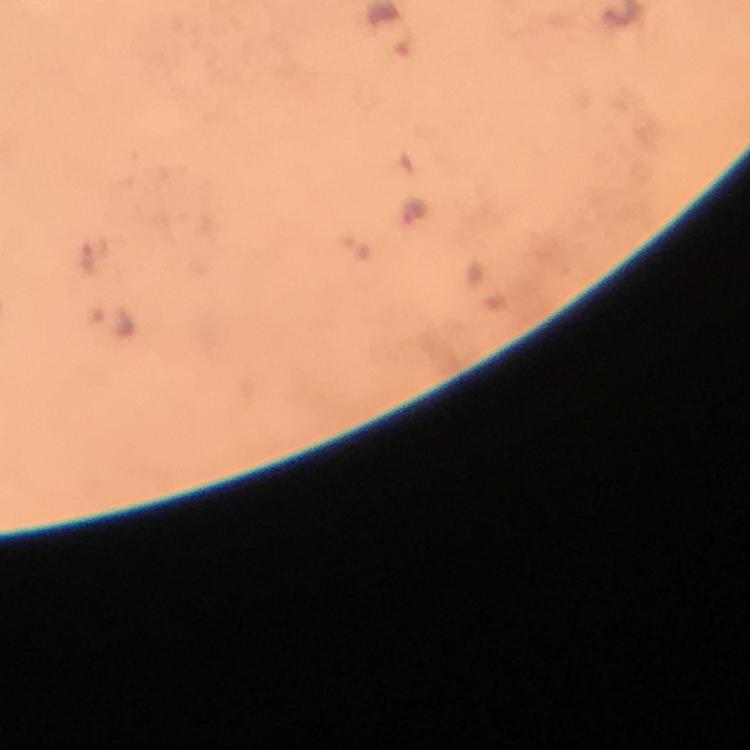
image size = 750×750 pixels
context = from a diagnostic examination for malaria
magnification = 100x
malaria parasite locations = approximate centers as {x, y} in pixels: {413, 216}, {115, 323}
immersion oil = used
preparation = thick blood film
stain = Giemsa
capture = smartphone mounted on the microscope
cropped from = one field of view